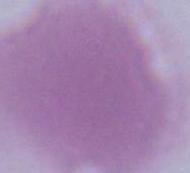

identification = erythrocyte
magnification = 1000x
modality = photomicrograph